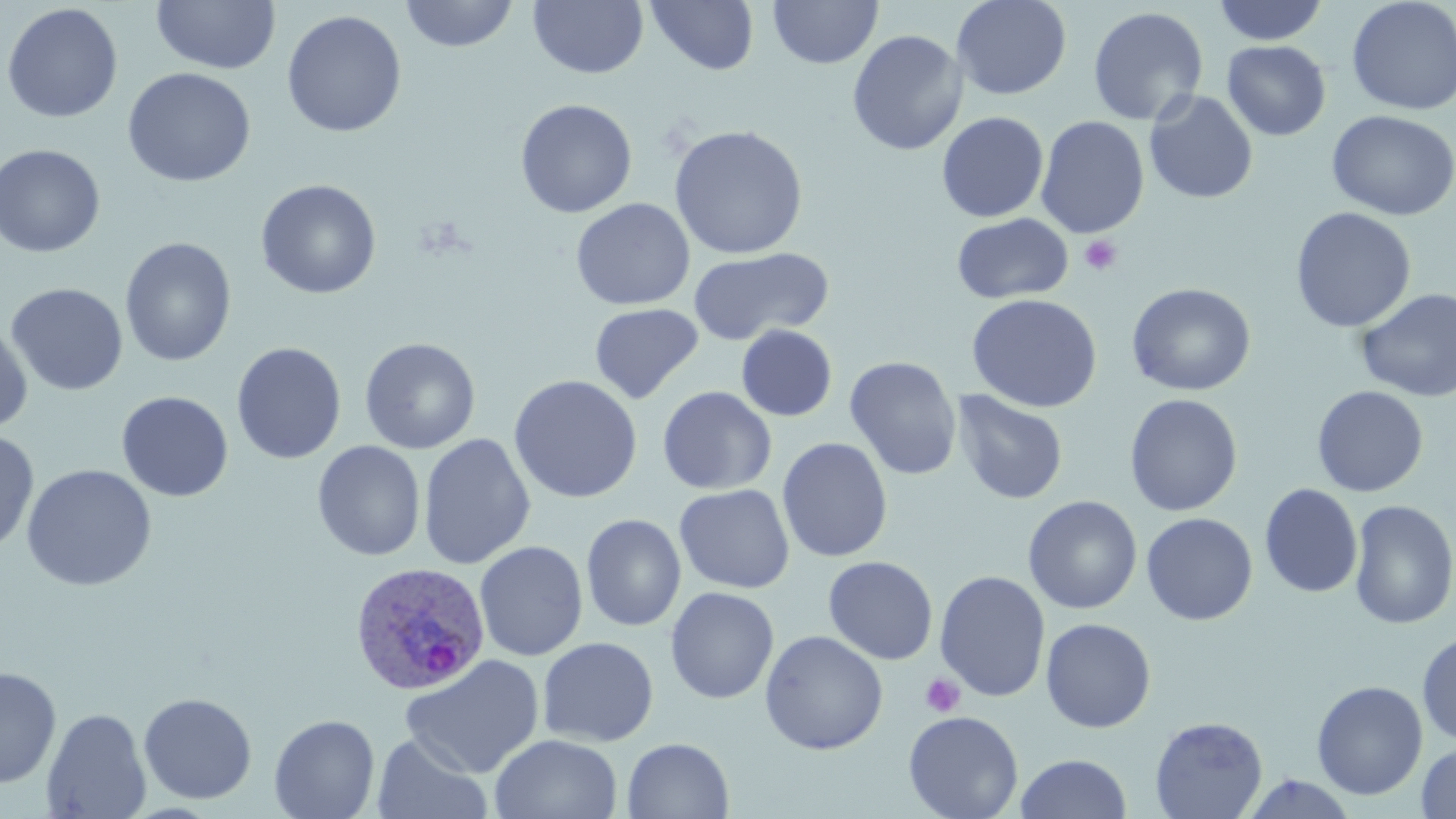

{
  "slide_level_diagnosis": "Plasmodium ovale",
  "uninfected_red_blood_cell_locations": "approximate bounding boxes as [x1, y1, x2, y2] in pixels: [151, 0, 281, 74], [400, 0, 519, 52], [646, 0, 760, 76], [951, 0, 1072, 100], [1212, 0, 1329, 45], [1346, 0, 1456, 116], [528, 1, 649, 79], [767, 1, 882, 70], [1, 2, 123, 124], [1088, 6, 1209, 125], [282, 10, 406, 137], [847, 29, 967, 156], [1223, 40, 1331, 141], [122, 67, 256, 188], [1144, 90, 1258, 204], [515, 98, 638, 218], [1326, 109, 1455, 221], [936, 111, 1049, 223], [1035, 116, 1150, 238], [669, 124, 808, 259], [0, 143, 106, 258], [255, 179, 381, 299], [570, 198, 695, 310], [1290, 207, 1417, 333], [951, 212, 1074, 304], [119, 237, 237, 367], [688, 247, 833, 345], [5, 282, 129, 396], [1127, 282, 1256, 396], [1355, 287, 1456, 403], [966, 293, 1103, 412], [589, 303, 704, 403], [0, 320, 33, 433], [736, 325, 837, 421], [359, 337, 481, 454], [231, 342, 346, 464], [844, 356, 962, 481], [508, 374, 643, 504], [1312, 385, 1428, 497], [657, 386, 776, 495], [952, 389, 1068, 505], [116, 391, 233, 502], [1124, 393, 1243, 516], [0, 429, 39, 556], [418, 433, 536, 570], [777, 437, 893, 562], [312, 441, 425, 561], [20, 464, 158, 591], [1259, 483, 1363, 598], [674, 484, 795, 594], [1023, 495, 1142, 614], [1348, 499, 1456, 630], [1141, 512, 1258, 625], [582, 513, 686, 632], [475, 541, 588, 661], [823, 556, 938, 665], [934, 570, 1051, 702], [665, 586, 780, 704], [1040, 618, 1156, 733], [759, 630, 888, 755], [1417, 630, 1456, 745], [537, 636, 659, 747], [400, 654, 545, 778], [0, 666, 61, 788], [1311, 680, 1428, 800], [138, 692, 258, 804], [41, 707, 152, 819], [903, 710, 1023, 819], [269, 714, 380, 819], [1149, 716, 1268, 819], [372, 732, 492, 819], [490, 733, 623, 819], [621, 737, 734, 819], [1416, 741, 1456, 818], [1015, 753, 1132, 819], [1241, 773, 1360, 818]",
  "platelet_locations": "approximate bounding boxes as [x1, y1, x2, y2] in pixels: [1079, 235, 1122, 276], [921, 673, 965, 717]",
  "preparation": "thin blood film",
  "magnification": "1000x",
  "image_size": "1456×819 pixels",
  "stain": "May-Grünwald-Giemsa",
  "field_of_view": "single",
  "plasmodium_ovale_infected_red_blood_cell_locations": "approximate bounding boxes as [x1, y1, x2, y2] in pixels: [348, 562, 491, 695]",
  "modality": "optical microscopy"
}